Name the blood parasite species.
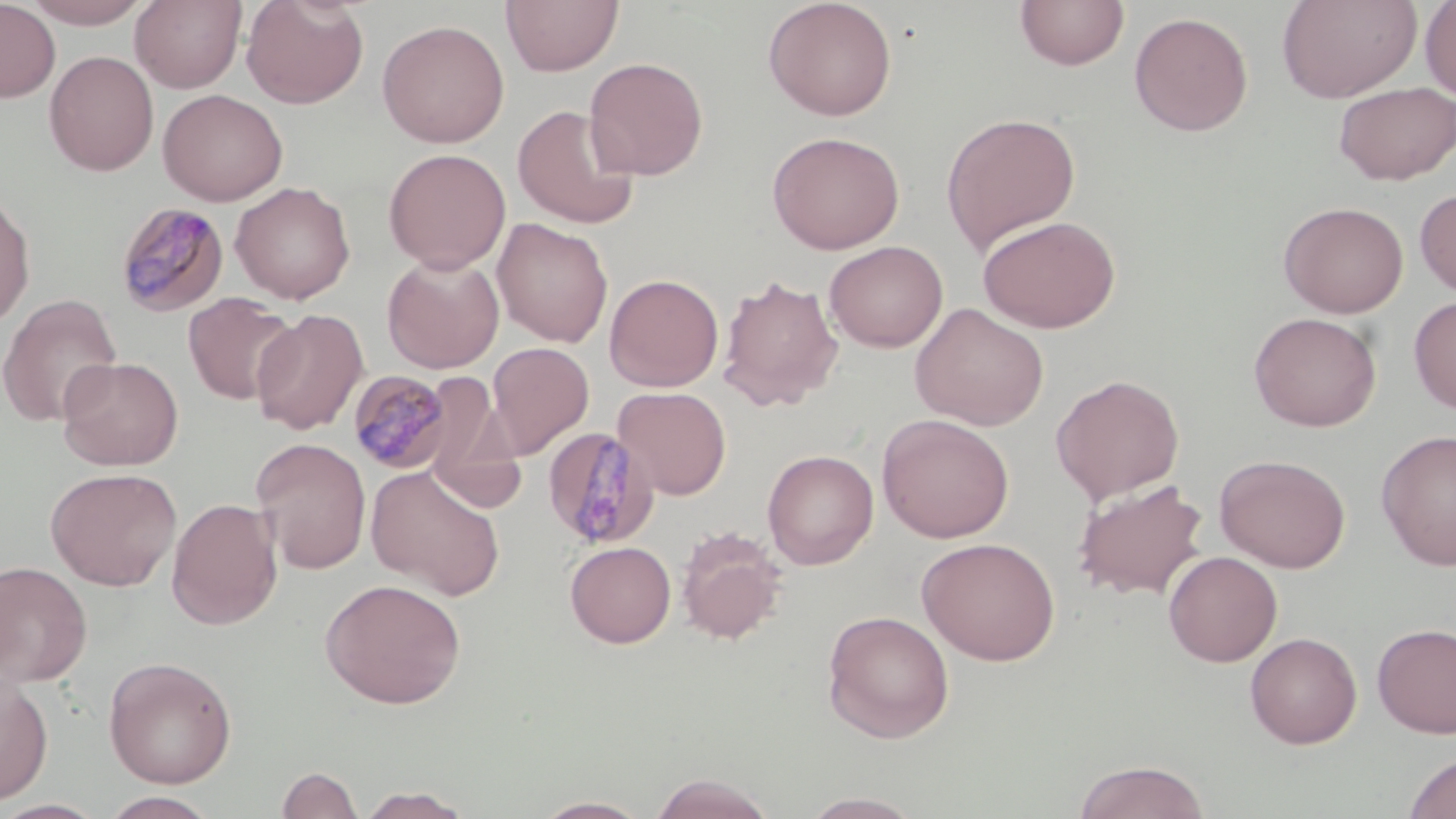

Plasmodium malariae.

magnification = 1000x
Plasmodium malariae-infected red blood cell locations (subset) = approximate bounding boxes as named x1/y1/x2/y2 corners in pixels: (x1=114, y1=200, x2=230, y2=318), (x1=348, y1=370, x2=454, y2=473)
uninfected red blood cell locations (subset) = approximate bounding boxes as named x1/y1/x2/y2 corners in pixels: (x1=20, y1=0, x2=155, y2=28), (x1=130, y1=0, x2=247, y2=92), (x1=241, y1=0, x2=369, y2=109), (x1=501, y1=0, x2=624, y2=75), (x1=763, y1=0, x2=898, y2=121), (x1=1014, y1=0, x2=1129, y2=71), (x1=1277, y1=0, x2=1421, y2=103), (x1=0, y1=1, x2=61, y2=103), (x1=1420, y1=1, x2=1456, y2=102), (x1=1128, y1=11, x2=1254, y2=136), (x1=376, y1=19, x2=510, y2=148), (x1=44, y1=51, x2=159, y2=176), (x1=584, y1=57, x2=708, y2=180), (x1=1333, y1=81, x2=1456, y2=185), (x1=157, y1=88, x2=287, y2=206), (x1=512, y1=104, x2=639, y2=230), (x1=940, y1=112, x2=1081, y2=255), (x1=767, y1=130, x2=905, y2=254), (x1=383, y1=148, x2=510, y2=273), (x1=230, y1=181, x2=355, y2=304), (x1=1414, y1=187, x2=1456, y2=298), (x1=0, y1=190, x2=36, y2=330), (x1=1278, y1=201, x2=1409, y2=318), (x1=1269, y1=202, x2=1398, y2=438), (x1=977, y1=214, x2=1121, y2=333), (x1=492, y1=218, x2=613, y2=347), (x1=824, y1=240, x2=948, y2=352), (x1=382, y1=253, x2=503, y2=373), (x1=604, y1=273, x2=724, y2=392), (x1=717, y1=275, x2=843, y2=410), (x1=0, y1=293, x2=122, y2=426), (x1=182, y1=293, x2=300, y2=406), (x1=1408, y1=295, x2=1456, y2=414), (x1=910, y1=303, x2=1049, y2=431), (x1=251, y1=309, x2=368, y2=434), (x1=1248, y1=311, x2=1382, y2=432), (x1=487, y1=342, x2=594, y2=458), (x1=57, y1=356, x2=184, y2=471), (x1=1050, y1=373, x2=1185, y2=504), (x1=613, y1=386, x2=732, y2=500), (x1=427, y1=410, x2=527, y2=515), (x1=877, y1=414, x2=1015, y2=543), (x1=1375, y1=430, x2=1456, y2=570), (x1=251, y1=438, x2=372, y2=574), (x1=762, y1=449, x2=879, y2=570), (x1=1215, y1=453, x2=1351, y2=573), (x1=366, y1=465, x2=505, y2=600), (x1=45, y1=467, x2=182, y2=591), (x1=1072, y1=478, x2=1209, y2=600), (x1=167, y1=498, x2=283, y2=631), (x1=676, y1=527, x2=788, y2=645), (x1=916, y1=536, x2=1061, y2=666), (x1=565, y1=541, x2=676, y2=648), (x1=1163, y1=550, x2=1282, y2=667), (x1=0, y1=560, x2=93, y2=687), (x1=319, y1=578, x2=466, y2=709), (x1=822, y1=610, x2=955, y2=743), (x1=1372, y1=622, x2=1456, y2=738), (x1=1245, y1=632, x2=1363, y2=748), (x1=103, y1=656, x2=238, y2=788), (x1=0, y1=672, x2=54, y2=806), (x1=1401, y1=752, x2=1456, y2=819), (x1=1072, y1=759, x2=1211, y2=819), (x1=276, y1=765, x2=364, y2=819), (x1=647, y1=773, x2=777, y2=818), (x1=353, y1=786, x2=475, y2=818), (x1=101, y1=791, x2=220, y2=818), (x1=798, y1=792, x2=927, y2=818), (x1=530, y1=795, x2=654, y2=818), (x1=0, y1=799, x2=109, y2=818)
image size = 1456×819 pixels
modality = optical microscopy
field of view = single
preparation = thin blood film
stain = May-Grünwald-Giemsa